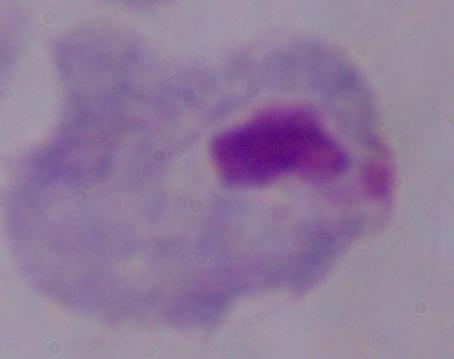
Captured at 1000x magnification. A trichomonad is shown. Micrograph.